Locate leukocytes (white blood cells).
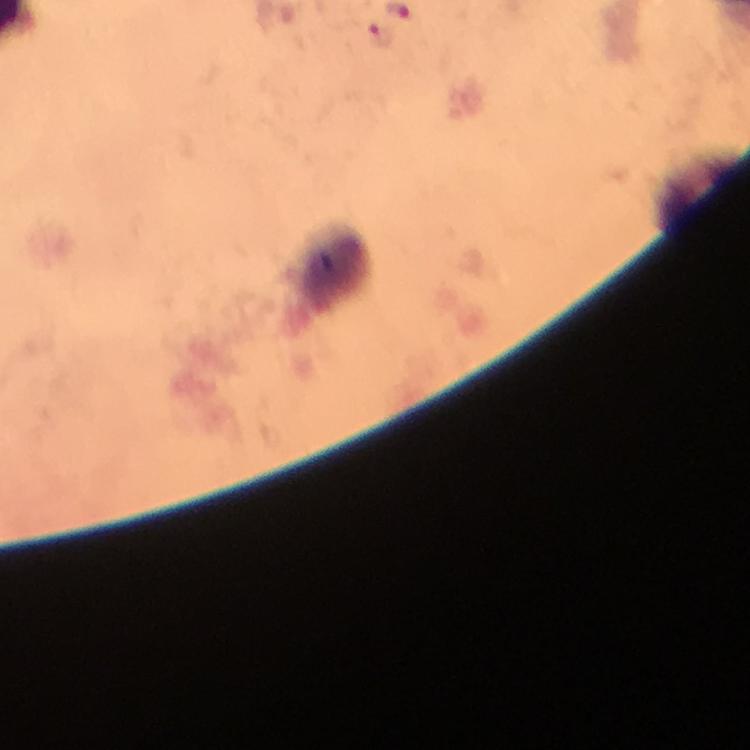

Approximate centers as (x, y) in pixels.
Leukocytes: (331, 272).

Malaria parasite locations: (380, 35). At 100x magnification. Immersion oil applied. A crop from one field of view. Photographed with a smartphone mounted on the microscope. Thick blood film. From a diagnostic examination for malaria. Giemsa-stained preparation. Image is 750×750 pixels.